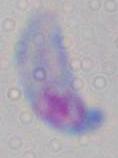
modality = photomicrograph
magnification = 1000x
identification = Toxoplasma gondii